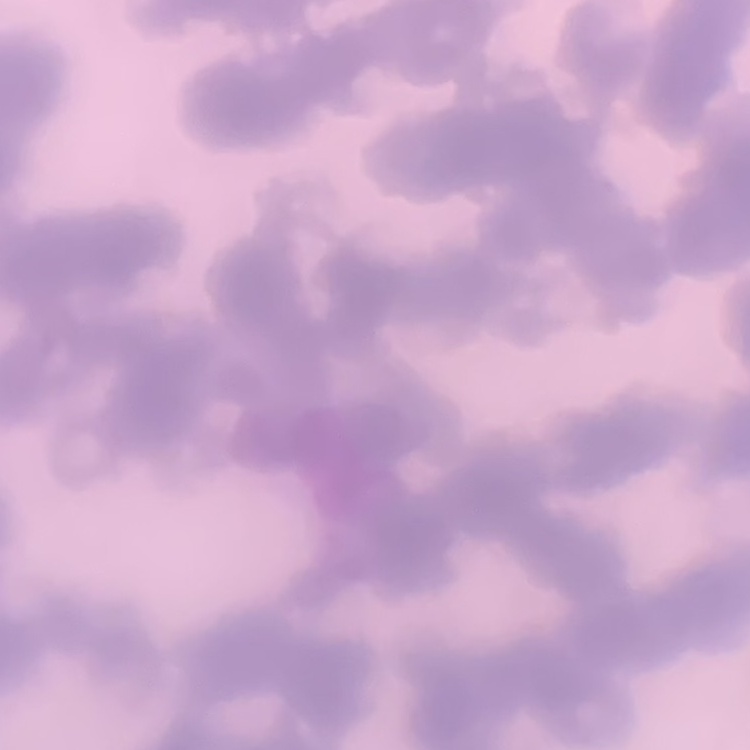
The red blood cells show rouleaux formation. Thin blood smear. Stained with either Field's or Giemsa. Square crop of a larger photomicrograph.